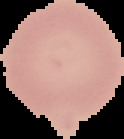

image type = segmented cell region with the area outside set to black
preparation = thin blood film
image size = 124×139 pixels
result = no Plasmodium parasites seen